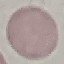

Result: negative for malaria parasites. Giemsa stain. Cell patch, automatically extracted from a larger field of view and resized to 64 × 64 pixels. Thin smear of blood. Photographed with a smartphone camera at the microscope eyepiece.